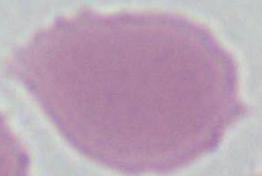
magnification = 1000x
modality = photomicrograph
identification = red blood cell